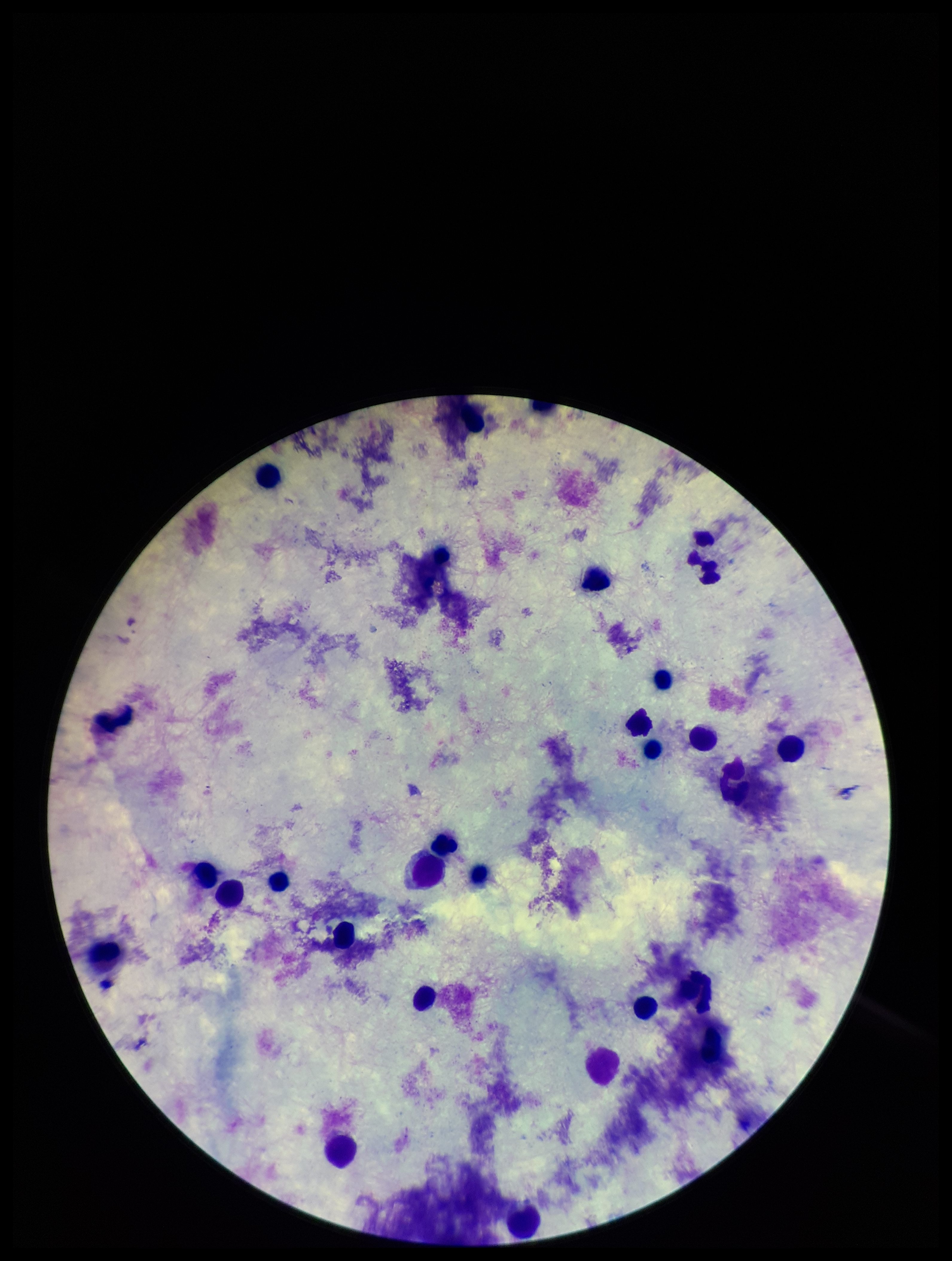

Summary:
  - Capture: smartphone photograph through the microscope eyepiece
  - Parasite count: 0
  - Field of view: one from this slide
  - Plasmodium parasites: none identified
  - Leukocyte count: 25
  - Stain: Giemsa
  - Patient malaria status: negative
  - Image size: 952×1261 pixels
  - Preparation: thick smear